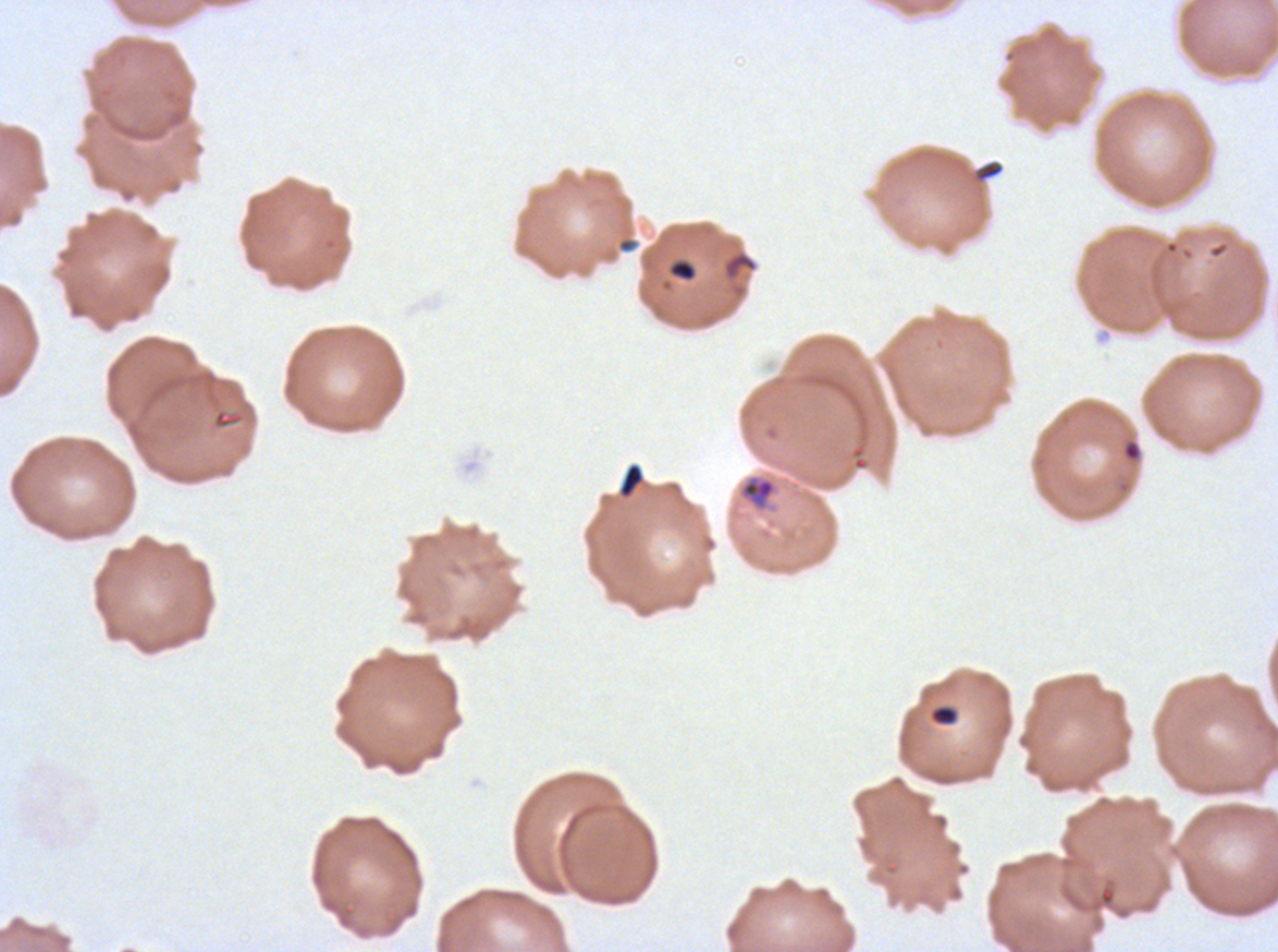

Approximate bounding rectangles given as corner coordinates in pixels from the top-left.
Summary:
  - Debris locations: (x1=975, y1=160, x2=1004, y2=183), (x1=618, y1=463, x2=645, y2=498), (x1=929, y1=704, x2=959, y2=726)
  - Ring locations: (x1=722, y1=251, x2=758, y2=281), (x1=1123, y1=441, x2=1141, y2=461), (x1=741, y1=477, x2=776, y2=508)
  - Stain: Giemsa
  - Preparation: thin blood film
  - Field of view: one sub-image of a larger composite
  - Image size: 1278×952 pixels
  - Specimen: P. falciparum from a patient in The Gambia, cultured ex vivo for 24 to 48 hours